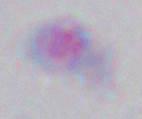
{
  "modality": "photomicrograph",
  "magnification": "1000x",
  "identification": "Toxoplasma gondii"
}